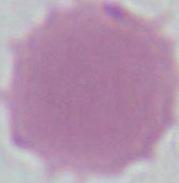
magnification: 1000x
modality: micrograph
identification: erythrocyte